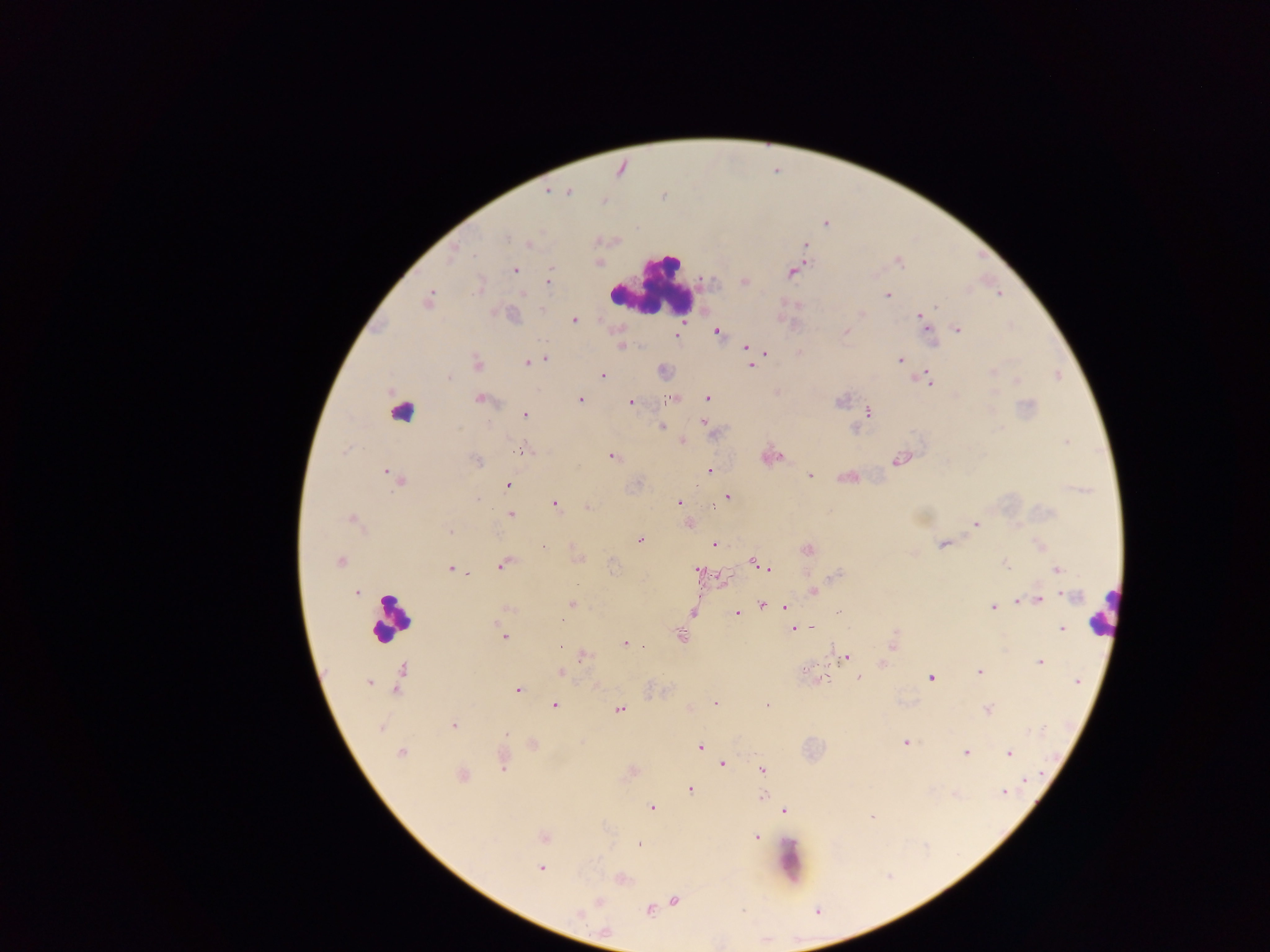

Approximate centers as (x, y) in pixels. Leukocyte locations: (651, 287), (403, 413), (1103, 611), (390, 616), (792, 860). Plasmodium parasite locations: (547, 191), (567, 191), (603, 201), (826, 224), (506, 238), (529, 244), (806, 245), (899, 263), (515, 271), (791, 272), (548, 282), (744, 282), (523, 293), (999, 294), (887, 295), (428, 299), (935, 307), (542, 310), (861, 314), (512, 315), (920, 315), (574, 320), (924, 322), (958, 330), (718, 332), (846, 333), (676, 335), (621, 346), (745, 347), (800, 352), (765, 353), (545, 358), (536, 360), (899, 360), (527, 362), (476, 363), (751, 366), (992, 372), (603, 376), (448, 379), (929, 380), (1017, 380), (708, 398), (481, 399), (580, 399), (669, 400), (630, 402), (1028, 406), (869, 413), (525, 414), (703, 422), (661, 427), (682, 441), (1067, 442), (525, 450), (611, 457), (898, 460), (477, 461), (709, 470), (810, 476), (849, 477), (398, 480), (509, 485), (728, 498), (477, 500), (679, 501), (555, 504), (588, 507), (511, 514), (352, 519), (976, 525), (449, 532), (639, 540), (943, 544), (1040, 544), (715, 545), (544, 547), (808, 549), (339, 562), (504, 564), (757, 564), (1006, 564), (768, 567), (450, 570), (1057, 570), (700, 571), (465, 573), (836, 575), (577, 585), (814, 591), (356, 593), (1071, 596), (1038, 600), (572, 605), (761, 605), (785, 607), (993, 607), (508, 609), (838, 611), (693, 612), (737, 613), (811, 627), (794, 629), (1062, 629), (680, 635), (504, 636), (625, 644), (893, 644), (561, 647), (584, 656), (846, 658), (1040, 662), (805, 670), (980, 672), (561, 673), (859, 677), (931, 677), (1077, 681), (368, 682), (396, 689), (517, 690), (715, 703), (555, 705), (767, 705), (618, 709), (987, 709), (453, 725), (380, 728), (506, 735), (905, 743), (700, 746), (400, 753), (965, 753), (1009, 754), (722, 763), (503, 767), (763, 770), (463, 775), (1026, 781), (691, 790), (1005, 792), (955, 795), (762, 796), (652, 807), (785, 810), (872, 817), (756, 837), (544, 838), (638, 844), (540, 868), (675, 900), (599, 902), (650, 910), (578, 913). Thick blood smear. One field of view. Photographed through a microscope with a mobile-phone camera. Image is 1270×952 pixels. Sample from Ghana.